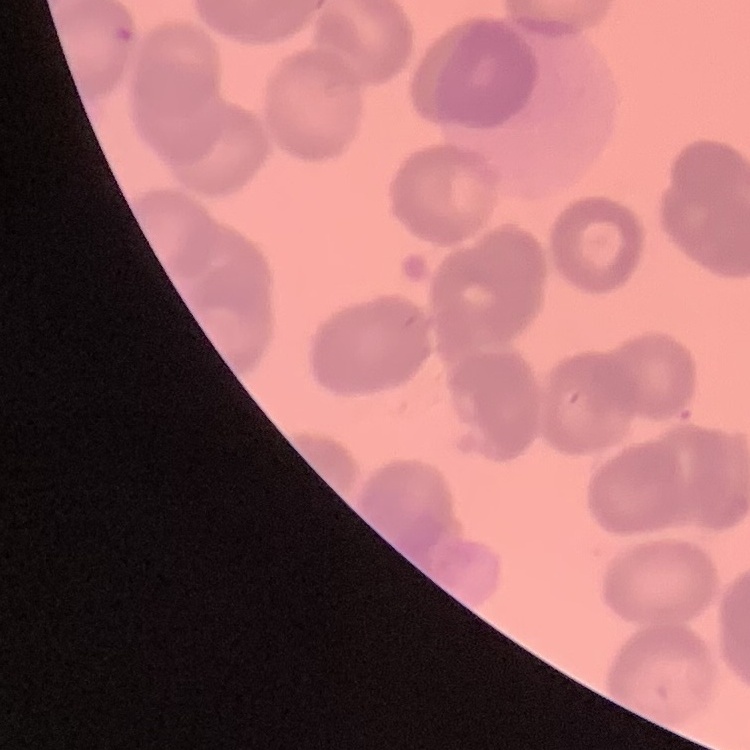

The erythrocytes exhibit rouleaux formation. Square crop of a larger photomicrograph. Field's or Giemsa stain. Thin peripheral smear.